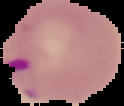
Segmented cell region on a black background. Image is 124×106 pixels. Malaria status: parasitized. From a thin blood smear.